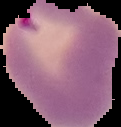
Cell region segmented out of the field of view; the surrounding area is masked to black. Image is 121×127 pixels. Malaria status: parasitized. From a thin blood smear.